Assess this cell for malaria.
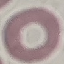
It is uninfected.

preparation = thin blood smear
image type = automatically extracted cell patch, resized to 64 × 64 pixels
stain = Giemsa
capture = smartphone through the microscope eyepiece